Report the malaria status of this cell.
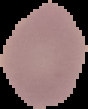

Uninfected.

preparation = thin blood smear
image size = 88×109 pixels
image type = segmented cell region on a black background